Outline each Plasmodium malariae-infected red blood cell.
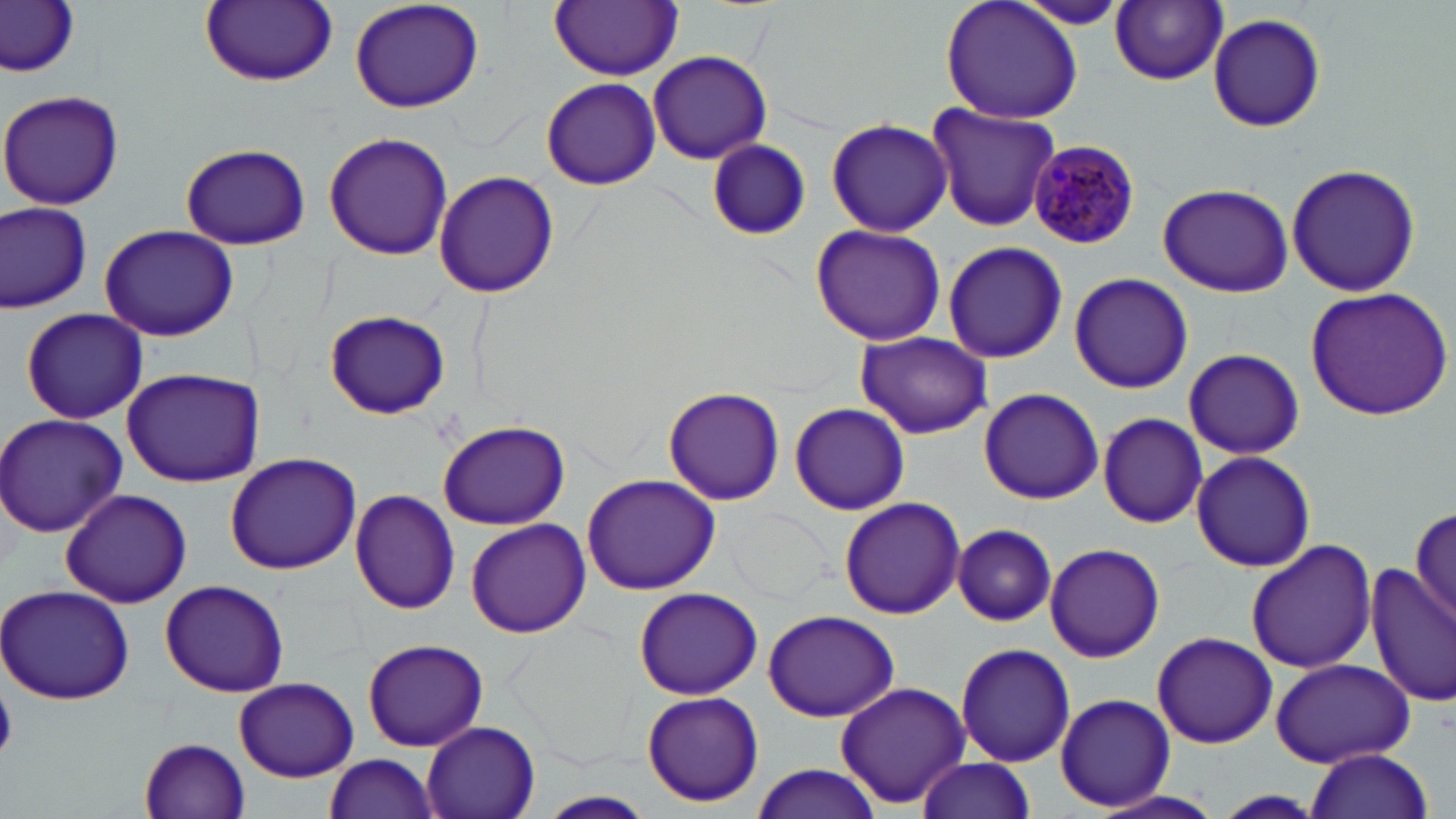
Approximate bounding boxes as (x1,y1)-(x2,y2) corner pairs in pixels.
Plasmodium malariae-infected red blood cells: (1028,140)-(1141,251).

slide-level diagnosis = Plasmodium malariae
field of view = single
modality = optical microscopy
magnification = 1000x
stain = May-Grünwald-Giemsa
image size = 1456×819 pixels
uninfected red blood cell locations = approximate bounding boxes as (x1,y1)-(x2,y2) corner pairs in pixels: (0,0)-(80,74), (347,0)-(486,113), (940,0)-(1085,125), (199,1)-(337,87), (551,1)-(683,80), (1111,1)-(1228,85), (1009,3)-(1135,30), (1208,12)-(1326,134), (648,50)-(772,165), (540,76)-(661,191), (1,90)-(125,210), (923,102)-(1062,231), (826,117)-(953,237), (323,131)-(454,261), (704,140)-(810,240), (180,142)-(311,250), (1285,163)-(1422,297), (434,170)-(560,300), (1158,182)-(1294,297), (0,199)-(94,313), (98,225)-(239,340), (811,225)-(948,346), (943,240)-(1066,364), (1068,272)-(1193,395), (1302,286)-(1454,420), (19,306)-(149,425), (325,309)-(449,418), (854,330)-(991,437), (1182,348)-(1304,459), (119,368)-(261,486), (662,387)-(785,506), (979,388)-(1103,504), (789,403)-(909,514), (1095,412)-(1208,529), (0,413)-(126,537), (437,420)-(570,529), (1190,449)-(1317,573), (224,452)-(362,575), (581,472)-(721,595), (60,488)-(192,609), (350,489)-(461,614), (839,497)-(964,619), (1409,502)-(1456,627), (466,519)-(590,638), (953,524)-(1057,626), (1245,537)-(1377,674), (1043,542)-(1168,664), (1369,564)-(1455,708), (159,580)-(289,697), (0,583)-(136,706), (631,586)-(764,700), (760,608)-(901,720), (1150,630)-(1278,749), (362,638)-(488,752), (954,641)-(1076,767), (1267,657)-(1415,768), (233,677)-(358,782), (833,682)-(970,806), (639,690)-(766,806), (1053,693)-(1175,810), (420,720)-(542,819), (138,737)-(252,818), (1303,749)-(1434,819), (322,752)-(441,819), (914,755)-(1034,819), (749,763)-(884,818), (1081,791)-(1229,819), (1214,791)-(1327,819), (536,792)-(657,819)
preparation = thin blood smear
platelet locations = approximate bounding boxes as (x1,y1)-(x2,y2) corner pairs in pixels: (0,682)-(17,764)